Name the blood parasite species.
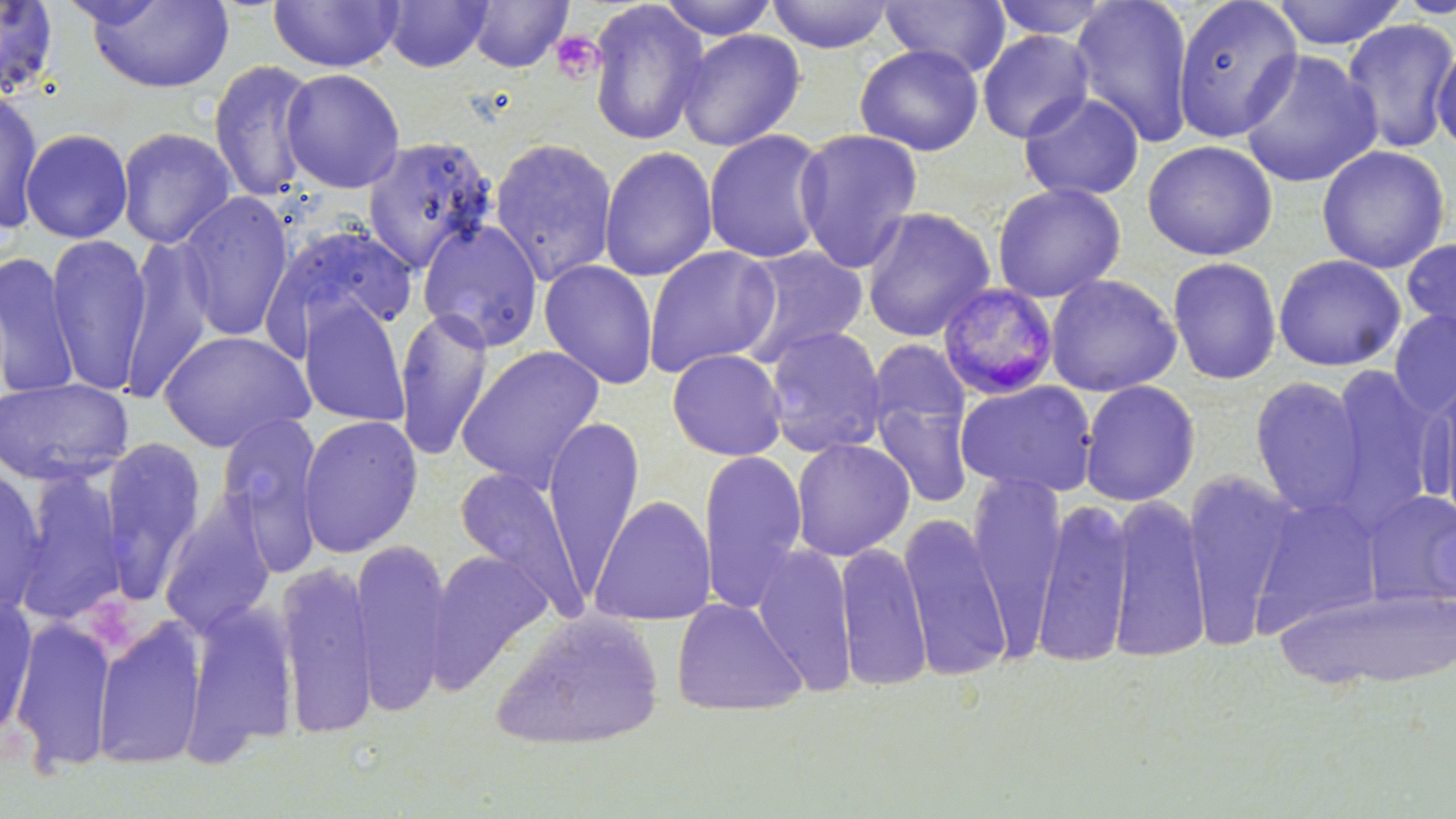
Plasmodium malariae.

Approximate bounding boxes as [x1, y1, x2, y2] in pixels. Platelet locations: [549, 30, 605, 84]. Uninfected red blood cell locations: [85, 0, 234, 94], [268, 0, 404, 73], [381, 0, 494, 72], [465, 0, 574, 73], [656, 0, 781, 40], [765, 0, 896, 53], [879, 0, 1012, 77], [989, 0, 1117, 41], [1069, 0, 1196, 147], [1172, 0, 1304, 144], [1269, 0, 1407, 50], [1393, 0, 1456, 19], [0, 1, 61, 101], [587, 2, 712, 147], [1341, 18, 1456, 154], [675, 28, 806, 152], [977, 29, 1094, 143], [1431, 41, 1456, 154], [854, 43, 984, 156], [1237, 49, 1382, 189], [207, 58, 319, 203], [279, 67, 406, 194], [0, 84, 44, 236], [1017, 90, 1146, 201], [116, 126, 238, 249], [19, 127, 134, 244], [792, 127, 924, 272], [702, 128, 831, 264], [361, 135, 499, 273], [488, 136, 619, 286], [1141, 139, 1278, 261], [1315, 144, 1452, 274], [598, 145, 718, 282], [990, 181, 1127, 302], [177, 190, 295, 343], [860, 205, 997, 343], [416, 218, 544, 352], [264, 220, 422, 350], [45, 233, 152, 395], [120, 233, 216, 401], [1401, 236, 1456, 345], [734, 244, 870, 365], [643, 245, 780, 378], [0, 250, 80, 400], [1273, 253, 1406, 372], [1166, 256, 1282, 385], [538, 259, 659, 389], [1044, 273, 1182, 397], [297, 297, 412, 428], [394, 307, 494, 460], [1388, 308, 1456, 420], [763, 325, 888, 458], [157, 328, 315, 453], [456, 345, 606, 492], [666, 348, 788, 462], [1322, 364, 1444, 530], [1248, 375, 1367, 517], [1421, 375, 1456, 521], [0, 377, 134, 488], [868, 377, 976, 512], [1078, 379, 1201, 506], [954, 380, 1099, 498], [215, 411, 326, 552], [297, 414, 423, 558], [542, 414, 644, 594], [99, 437, 209, 604], [790, 437, 915, 561], [698, 448, 809, 613], [0, 462, 48, 617], [13, 467, 129, 628], [454, 467, 588, 617], [1181, 470, 1300, 647], [967, 471, 1066, 658], [1361, 490, 1456, 608], [160, 494, 280, 637], [588, 494, 717, 626], [1249, 494, 1385, 635], [1106, 495, 1211, 663], [1032, 496, 1134, 669], [898, 511, 1012, 681], [352, 538, 451, 716], [835, 540, 932, 691], [752, 543, 857, 696], [425, 549, 553, 693], [275, 558, 379, 739], [1281, 585, 1455, 690], [1, 594, 38, 744], [671, 597, 807, 718], [181, 598, 300, 763], [489, 609, 665, 751], [9, 615, 116, 775], [92, 617, 207, 771]. Plasmodium malariae-infected red blood cell locations: [937, 282, 1060, 401]. Image is 1456×819 pixels. 1000x magnification. May-Grünwald-Giemsa-stained preparation. One field of a larger specimen. Light microscopy. Thin blood film.